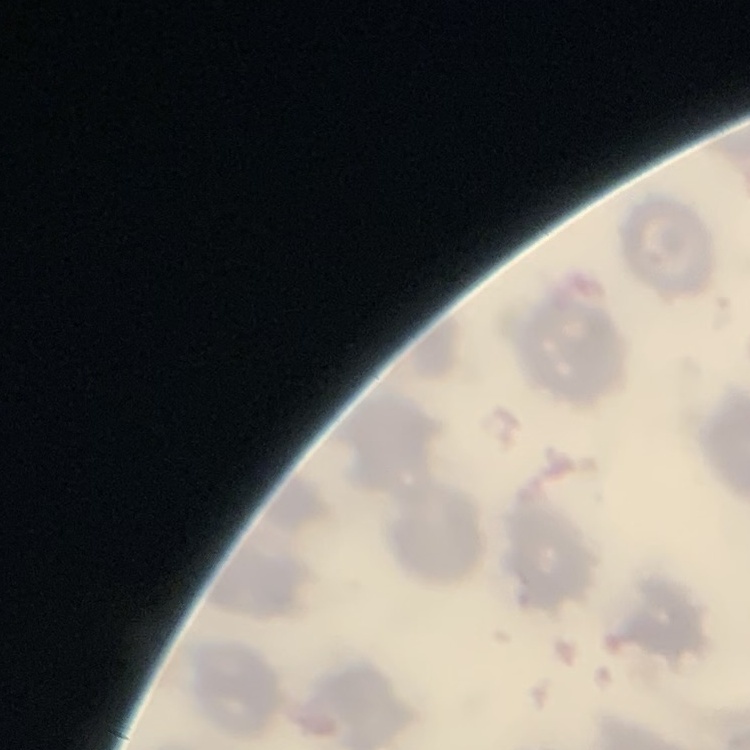

Summary:
  - Erythrocyte morphology: no rouleaux formation
  - Image type: square crop of a larger photomicrograph
  - Preparation: thin blood film
  - Stain: Field's or Giemsa